Locate every malaria parasite.
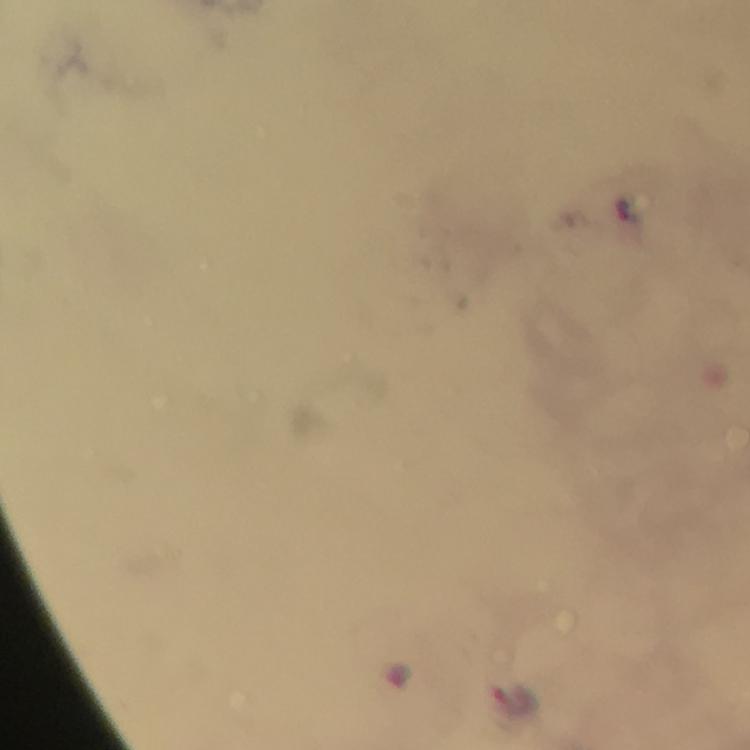
Approximate centers as (x, y) in pixels.
Malaria parasites: (625, 207).

cropped from = one field of view
context = from a diagnostic examination for malaria
image size = 750×750 pixels
immersion oil = used
capture = smartphone camera through the microscope
stain = Giemsa
preparation = thick smear
magnification = 100x